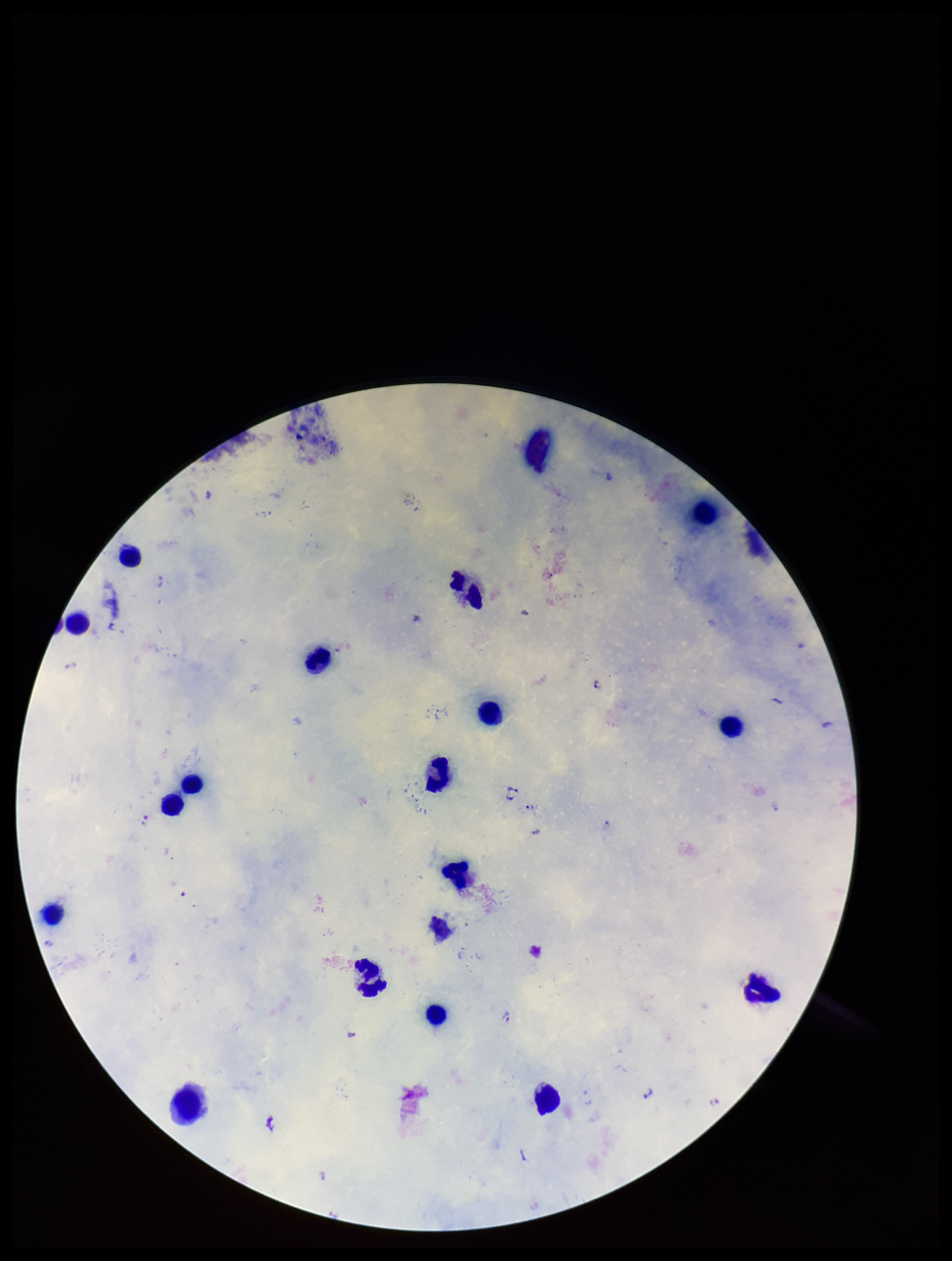

Summary:
  - Species reported for this patient: Plasmodium falciparum
  - Image size: 952×1261 pixels
  - Plasmodium parasites: detected
  - Field of view: single
  - Stain: Giemsa
  - Capture: smartphone photograph through the microscope eyepiece
  - Parasite count: 11
  - Preparation: thick
  - Patient malaria status: positive
  - Leukocyte count: 19